Classify this cell by malaria status.
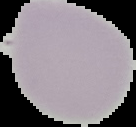
It is uninfected.

Summary:
  - Image type: segmented cell region with the area outside set to black
  - Image size: 136×127 pixels
  - Preparation: thin blood smear